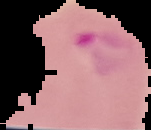
Cell region segmented out of the field of view; the surrounding area is masked to black. Result: Plasmodium parasites detected. From a thin blood film. Image is 151×130 pixels.